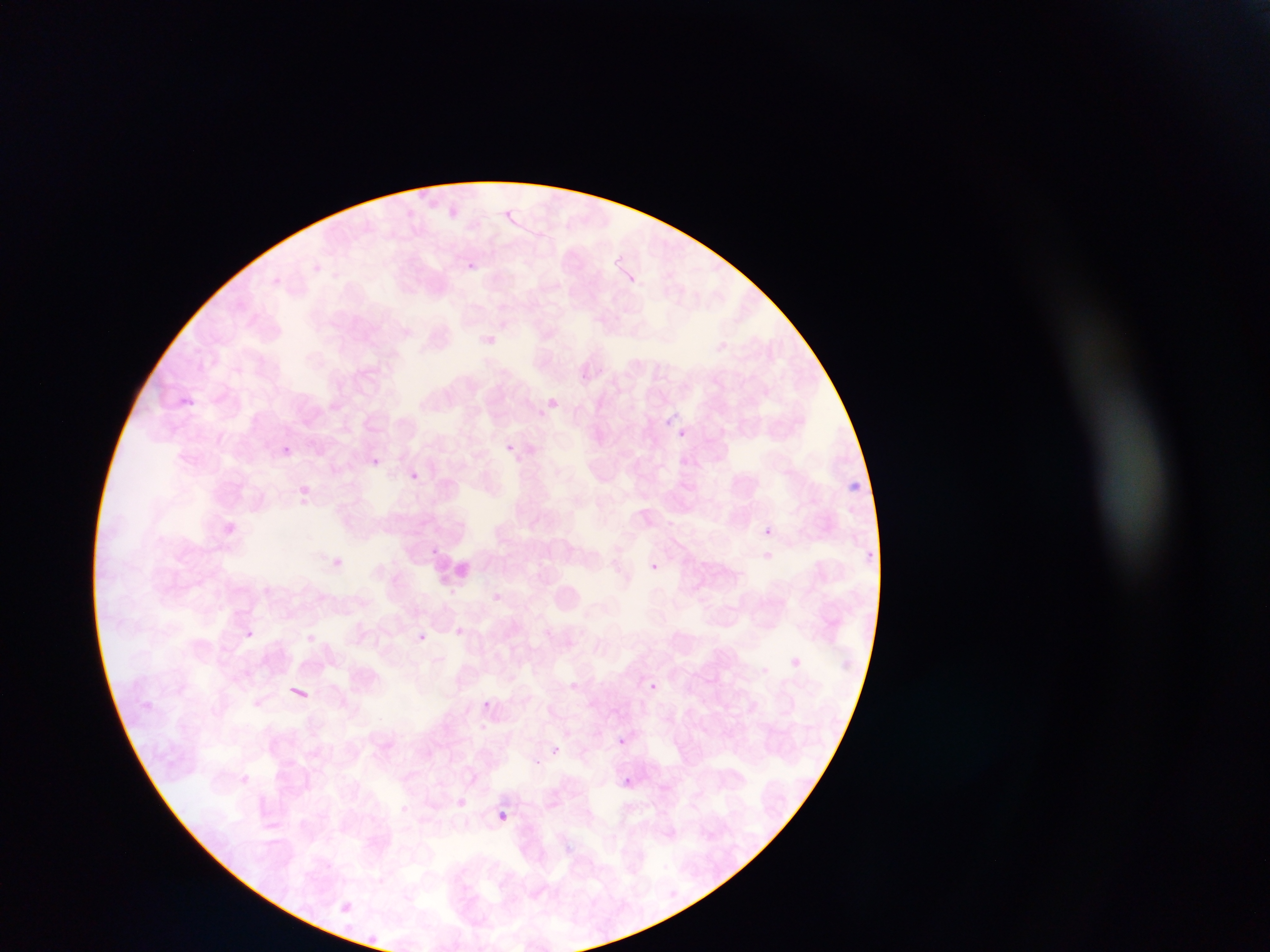
Approximate bounding boxes as (left, top, right, bottom) in pixels.
Summary:
  - Plasmodium parasite locations: (461, 255, 477, 277), (178, 394, 200, 409), (546, 395, 565, 406), (678, 428, 687, 434), (275, 439, 289, 454), (503, 439, 512, 450), (368, 457, 387, 469), (409, 466, 422, 483), (299, 479, 308, 492), (848, 480, 863, 492), (761, 525, 781, 534), (866, 546, 882, 555), (329, 556, 345, 569), (649, 561, 667, 577), (241, 625, 260, 636), (451, 626, 475, 635), (418, 634, 444, 650), (791, 652, 807, 664), (649, 680, 661, 689), (482, 695, 494, 708), (616, 732, 628, 751), (552, 743, 570, 762), (619, 774, 635, 790), (453, 793, 466, 811), (492, 806, 513, 826), (338, 897, 355, 909), (365, 928, 377, 947)
  - Leukocyte locations: (429, 549, 473, 593)
  - Capture: mobile-phone photograph through a microscope
  - Preparation: thin blood smear
  - Country: Ghana
  - Field of view: single
  - Image size: 1270×952 pixels